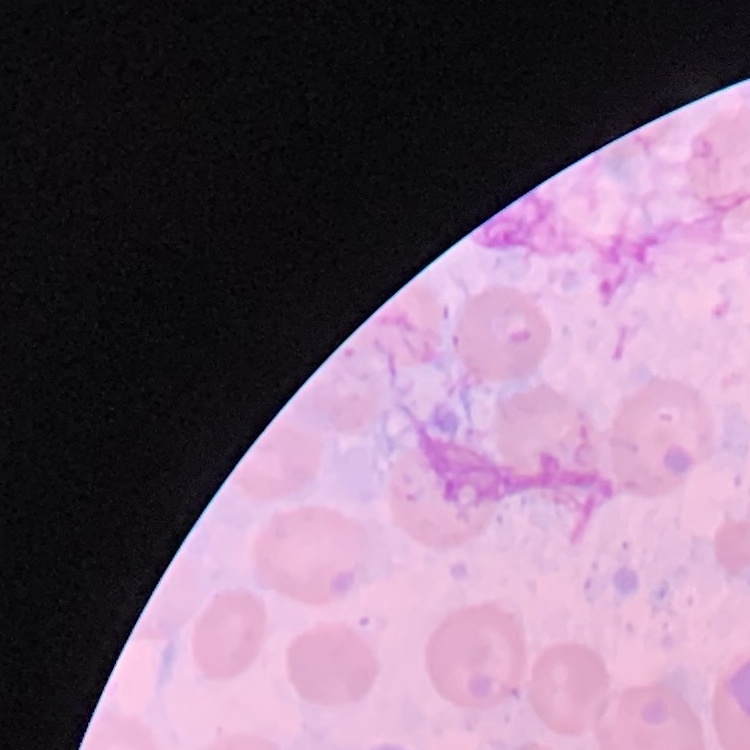
The red blood cells show no rouleaux formation. Field's or Giemsa stain. Thin blood smear. One tile cut from a larger photomicrograph.